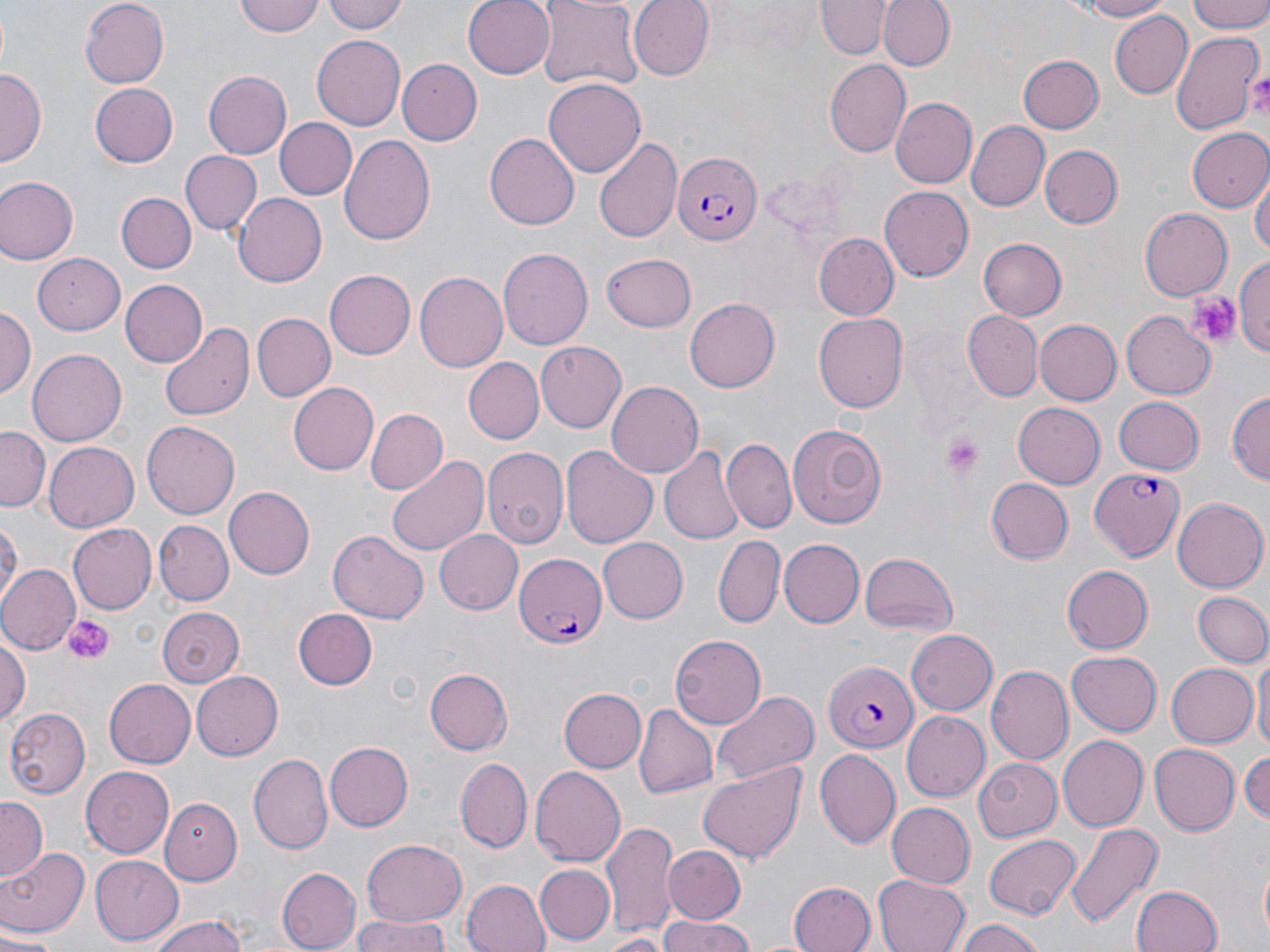
Approximate bounding boxes as (x1, y1, x2, y2) in pixels. Uninfected red blood cell locations: (234, 0, 323, 37), (324, 0, 410, 35), (461, 0, 556, 79), (628, 0, 716, 80), (813, 0, 889, 59), (878, 0, 953, 72), (1062, 0, 1176, 21), (1187, 0, 1270, 34), (80, 1, 169, 88), (535, 2, 644, 90), (1108, 10, 1192, 100), (1171, 32, 1263, 135), (312, 35, 405, 129), (1018, 55, 1104, 134), (824, 59, 910, 157), (396, 60, 483, 144), (0, 70, 44, 164), (203, 71, 291, 159), (545, 75, 645, 174), (90, 81, 177, 166), (890, 98, 974, 188), (273, 117, 356, 200), (965, 121, 1050, 213), (1186, 128, 1270, 209), (484, 132, 579, 230), (340, 134, 436, 246), (594, 136, 681, 243), (1040, 145, 1122, 229), (181, 151, 261, 234), (1253, 173, 1269, 265), (0, 176, 77, 264), (879, 186, 975, 282), (233, 191, 327, 284), (117, 192, 195, 273), (1140, 208, 1232, 300), (815, 233, 900, 321), (977, 237, 1067, 320), (498, 247, 594, 351), (31, 253, 125, 334), (602, 253, 697, 330), (1235, 258, 1270, 356), (324, 269, 415, 359), (416, 270, 511, 372), (120, 279, 208, 367), (684, 297, 780, 392), (0, 307, 35, 402), (965, 310, 1041, 400), (1121, 310, 1217, 397), (251, 313, 335, 401), (815, 313, 907, 412), (1034, 319, 1121, 404), (159, 321, 253, 422), (536, 342, 627, 430), (27, 349, 126, 446), (464, 358, 543, 443), (606, 381, 704, 479), (288, 383, 377, 474), (1228, 393, 1269, 490), (1112, 395, 1204, 474), (1013, 403, 1104, 488), (365, 407, 448, 496), (142, 420, 243, 520), (787, 421, 886, 529), (0, 427, 48, 510), (723, 440, 796, 534), (44, 443, 138, 530), (560, 445, 658, 548), (659, 445, 744, 546), (483, 446, 569, 549), (386, 453, 489, 559), (984, 479, 1073, 564), (224, 486, 314, 579), (1172, 495, 1269, 592), (0, 516, 20, 616), (155, 521, 233, 605), (67, 524, 157, 614), (329, 529, 429, 622), (436, 531, 522, 615), (714, 534, 786, 627), (596, 536, 688, 623), (777, 539, 864, 628), (861, 551, 959, 636), (0, 565, 80, 657), (1062, 566, 1153, 654), (1191, 592, 1270, 668), (157, 605, 244, 686), (294, 608, 377, 689), (906, 628, 997, 716), (0, 633, 29, 726), (670, 636, 767, 728), (1066, 650, 1162, 737), (1253, 656, 1269, 759), (1165, 662, 1259, 750), (986, 665, 1072, 763), (424, 666, 512, 755), (192, 671, 283, 759), (104, 678, 196, 768), (557, 685, 645, 773), (710, 688, 820, 784), (632, 705, 716, 801), (4, 706, 88, 797), (902, 711, 989, 800), (1058, 733, 1148, 832), (327, 741, 413, 832), (1150, 743, 1240, 834), (1244, 746, 1270, 825), (814, 749, 902, 848), (250, 751, 333, 857), (455, 757, 530, 851), (976, 759, 1063, 844), (697, 762, 807, 866), (530, 765, 626, 866), (81, 766, 174, 859), (160, 796, 243, 883), (0, 798, 46, 881), (886, 802, 974, 888), (602, 821, 675, 937), (1065, 822, 1162, 931), (983, 834, 1082, 918), (358, 840, 467, 929), (663, 846, 746, 924), (0, 848, 92, 941), (89, 856, 182, 944), (1257, 859, 1269, 946), (536, 863, 614, 943), (278, 867, 359, 951), (872, 874, 970, 952), (462, 877, 550, 952), (788, 882, 875, 952), (1131, 884, 1224, 952), (148, 915, 252, 952), (657, 915, 756, 952), (347, 917, 455, 952), (953, 918, 1048, 952), (1, 932, 58, 952), (596, 934, 669, 951). Plasmodium falciparum-infected red blood cell locations: (674, 152, 762, 247), (1088, 469, 1184, 563), (512, 553, 606, 648), (821, 659, 917, 752). Platelet locations: (1246, 69, 1270, 113), (1185, 288, 1243, 349), (939, 432, 987, 481), (64, 615, 114, 662). Slide-level diagnosis: Plasmodium falciparum. Optical microscopy. Single field of view. Image is 1270×952 pixels. 1000x magnification. Thin blood film. May-Grünwald-Giemsa stain.